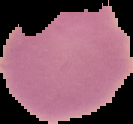
image type = cell region segmented out of the field of view; surrounding area masked to black
preparation = thin blood smear
malaria status = uninfected
image size = 133×124 pixels